State which parasite is depicted.
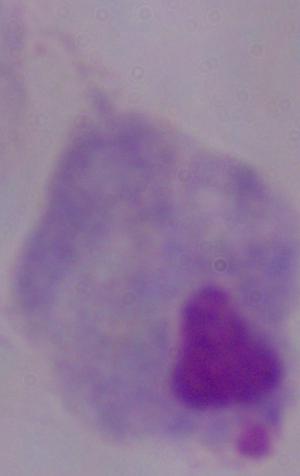

A trichomonad.

magnification = 1000x
modality = micrograph